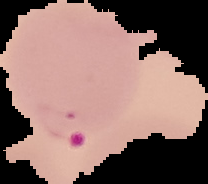
From a thin blood film. Image is 208×184 pixels. Result: Plasmodium parasites detected. The area outside the segmented cell region is set to black.